Report the malaria status of this cell.
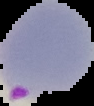
It is parasitized.

From a thin blood film. Image is 94×106 pixels. The area outside the segmented cell region is set to black.